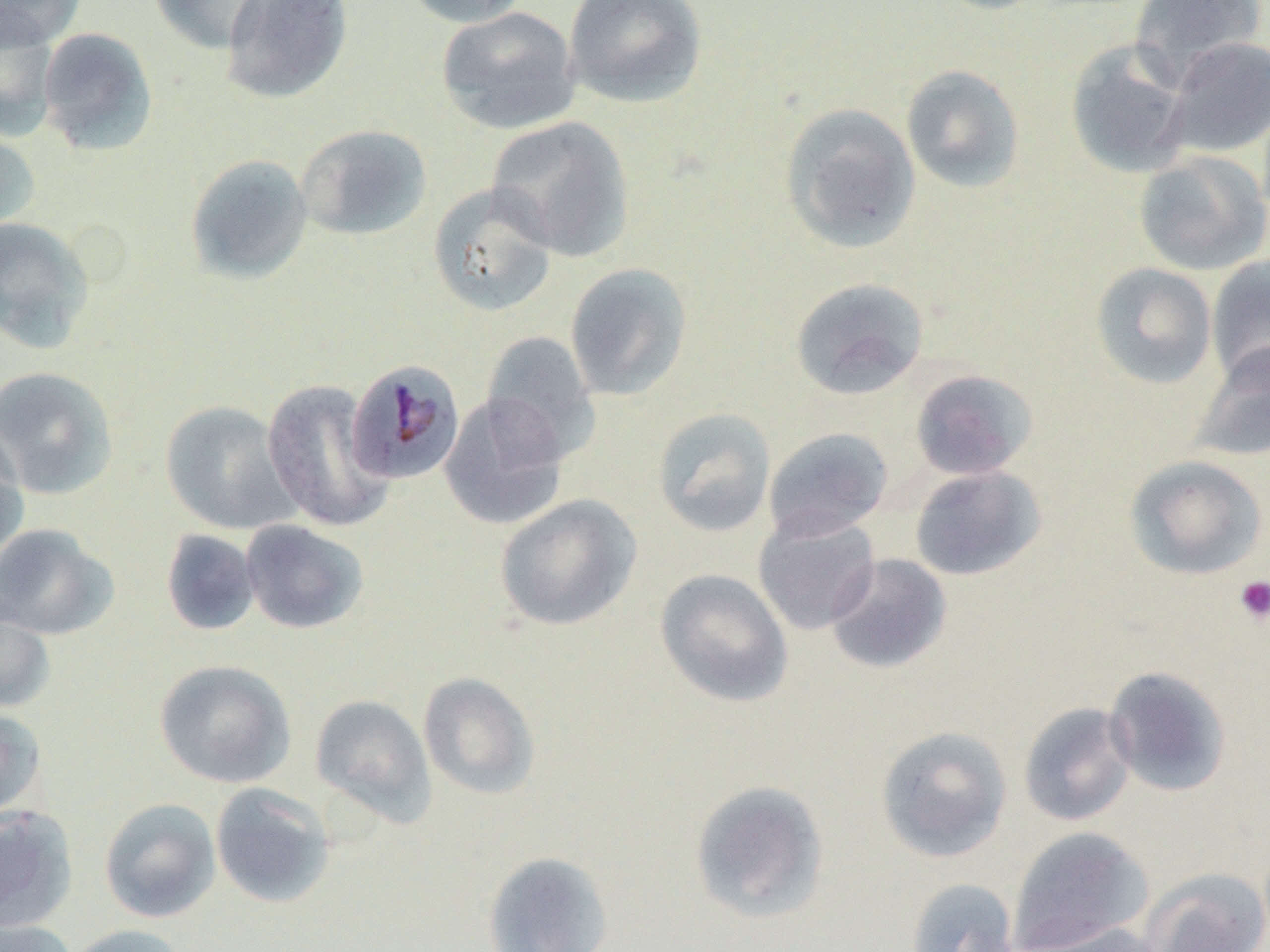

slide_level_diagnosis: Plasmodium malariae
field_of_view: one of a larger specimen
image_size: 1270×952 pixels
uninfected_red_blood_cell_locations: 'approximate bounding boxes as named x1/y1/x2/y2 corners in pixels: (x1=0, y1=0, x2=85, y2=50), (x1=148, y1=0, x2=270, y2=54), (x1=221, y1=0, x2=353, y2=104), (x1=400, y1=0, x2=532, y2=28), (x1=562, y1=0, x2=707, y2=108), (x1=929, y1=0, x2=1051, y2=14), (x1=1129, y1=0, x2=1265, y2=82), (x1=436, y1=6, x2=581, y2=135), (x1=0, y1=13, x2=60, y2=141), (x1=36, y1=27, x2=159, y2=156), (x1=1162, y1=36, x2=1270, y2=157), (x1=1065, y1=39, x2=1194, y2=179), (x1=900, y1=64, x2=1025, y2=193), (x1=779, y1=102, x2=921, y2=254), (x1=486, y1=116, x2=636, y2=261), (x1=296, y1=124, x2=432, y2=241), (x1=0, y1=126, x2=41, y2=235), (x1=1133, y1=150, x2=1270, y2=276), (x1=185, y1=154, x2=313, y2=284), (x1=427, y1=182, x2=559, y2=317), (x1=0, y1=216, x2=96, y2=353), (x1=1205, y1=255, x2=1270, y2=386), (x1=564, y1=262, x2=693, y2=401), (x1=1090, y1=262, x2=1218, y2=390), (x1=789, y1=277, x2=929, y2=400), (x1=480, y1=331, x2=601, y2=462), (x1=1188, y1=340, x2=1270, y2=462), (x1=0, y1=366, x2=119, y2=499), (x1=909, y1=368, x2=1039, y2=480), (x1=261, y1=378, x2=393, y2=533), (x1=438, y1=393, x2=570, y2=531), (x1=159, y1=400, x2=297, y2=535), (x1=652, y1=407, x2=776, y2=537), (x1=0, y1=425, x2=29, y2=568), (x1=763, y1=427, x2=893, y2=540), (x1=1124, y1=454, x2=1268, y2=581), (x1=909, y1=465, x2=1047, y2=581), (x1=494, y1=493, x2=642, y2=631), (x1=752, y1=511, x2=881, y2=635), (x1=239, y1=519, x2=369, y2=634), (x1=0, y1=523, x2=118, y2=640), (x1=160, y1=529, x2=261, y2=636), (x1=825, y1=553, x2=952, y2=674), (x1=654, y1=568, x2=794, y2=707), (x1=0, y1=604, x2=55, y2=714), (x1=154, y1=659, x2=296, y2=789), (x1=1102, y1=665, x2=1233, y2=797), (x1=417, y1=671, x2=541, y2=800), (x1=310, y1=694, x2=436, y2=826), (x1=1017, y1=702, x2=1137, y2=827), (x1=0, y1=707, x2=47, y2=820), (x1=875, y1=724, x2=1012, y2=862), (x1=689, y1=780, x2=829, y2=923), (x1=209, y1=782, x2=336, y2=908), (x1=98, y1=797, x2=221, y2=923), (x1=0, y1=806, x2=78, y2=931), (x1=1006, y1=827, x2=1155, y2=952), (x1=482, y1=850, x2=614, y2=952), (x1=1139, y1=867, x2=1270, y2=952), (x1=905, y1=877, x2=1019, y2=952), (x1=0, y1=918, x2=78, y2=952), (x1=1014, y1=921, x2=1168, y2=952), (x1=64, y1=924, x2=188, y2=952)'
preparation: thin blood smear
magnification: 1000x
modality: light microscopy
plasmodium_malariae_infected_red_blood_cell_locations: 'approximate bounding boxes as named x1/y1/x2/y2 corners in pixels: (x1=345, y1=359, x2=467, y2=485)'
platelet_locations: 'approximate bounding boxes as named x1/y1/x2/y2 corners in pixels: (x1=1233, y1=575, x2=1270, y2=626)'